Classify this cell by malaria status.
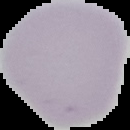

It is uninfected.

Summary:
  - Image type: segmented cell region on a black background
  - Preparation: thin blood film
  - Image size: 130×130 pixels